Evaluate for parasitized red blood cells.
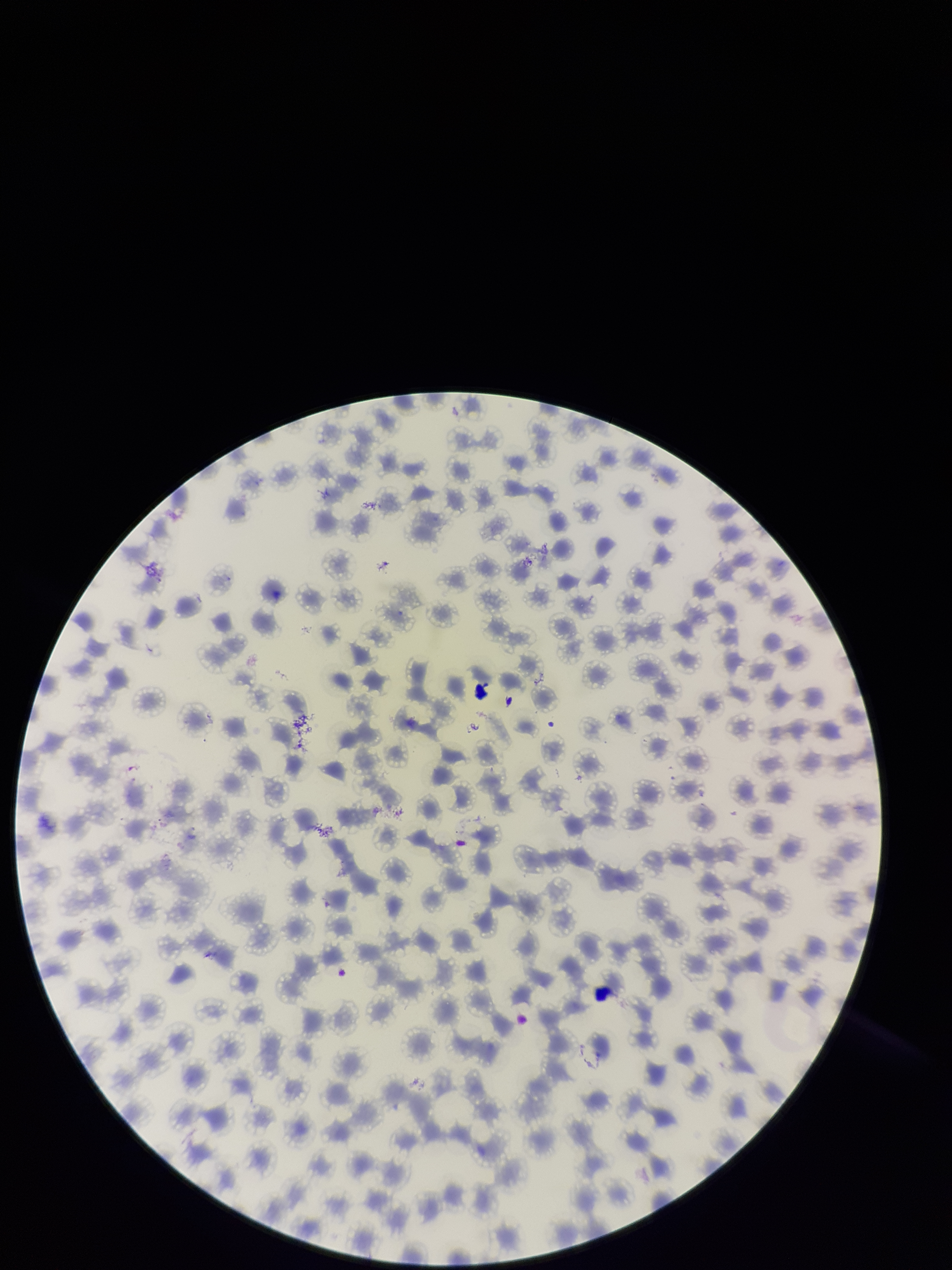

None identified.

image size = 952×1270 pixels
patient malaria status = infected
species reported for this patient = Plasmodium falciparum
stain = Giemsa
preparation = thin smear
capture = smartphone photograph through the microscope eyepiece
parasitized red blood cell count = 0
red blood cell count = 183
field of view = one from this slide